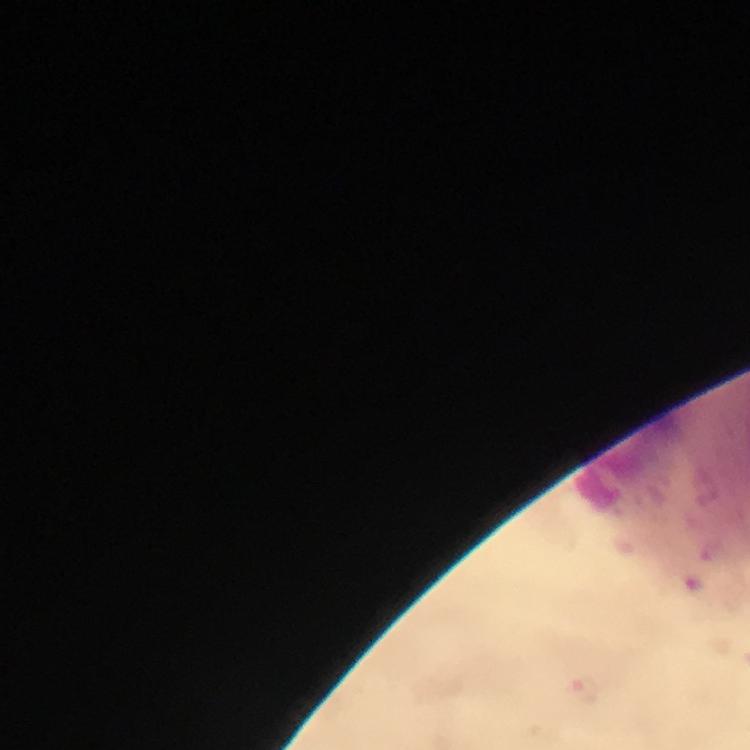

malaria parasite locations = approximate centers as [x, y] in pixels: [584, 689]
stain = Giemsa
preparation = thick smear
immersion oil = used
capture = smartphone camera through the microscope
image size = 750×750 pixels
magnification = 100x
cropped from = a single field of view
context = from a diagnostic examination for malaria